Locate every Plasmodium parasite.
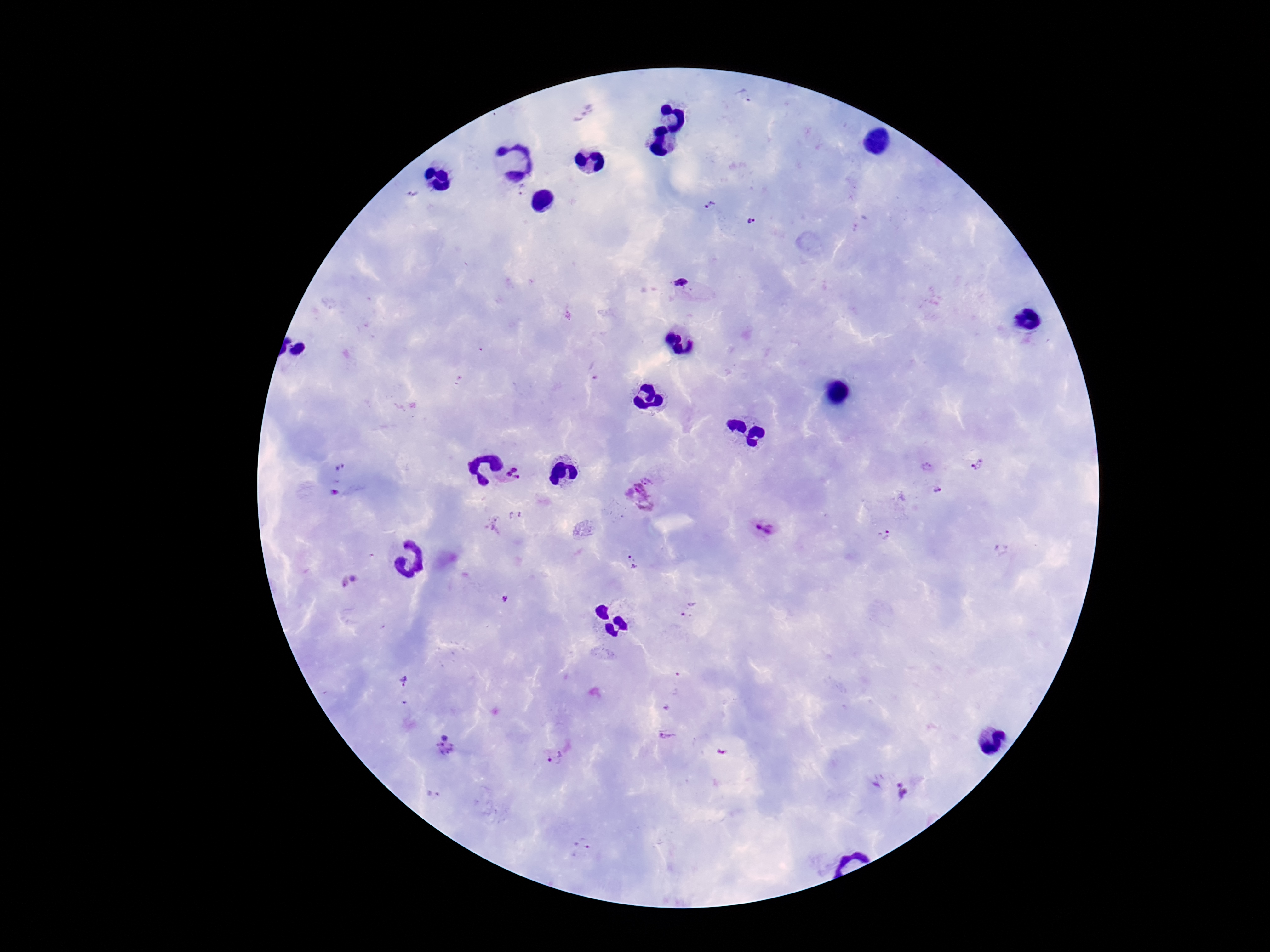

Approximate centers as (x, y) in pixels.
Plasmodium parasites: (747, 92), (525, 190), (711, 206), (754, 223), (689, 289), (977, 464), (929, 467), (341, 471), (513, 473), (937, 490), (336, 492), (641, 495), (493, 524), (764, 527), (884, 535), (1002, 548), (633, 562), (355, 578), (344, 582), (505, 598), (688, 609), (405, 680), (667, 707), (669, 735), (445, 746), (722, 751), (556, 756), (904, 790), (433, 795), (583, 846).

image size = 1270×952 pixels
magnification = 100x
stain = Giemsa
patient malaria status = positive
capture = smartphone camera through the microscope eyepiece
preparation = thick blood smear
field of view = one from this slide